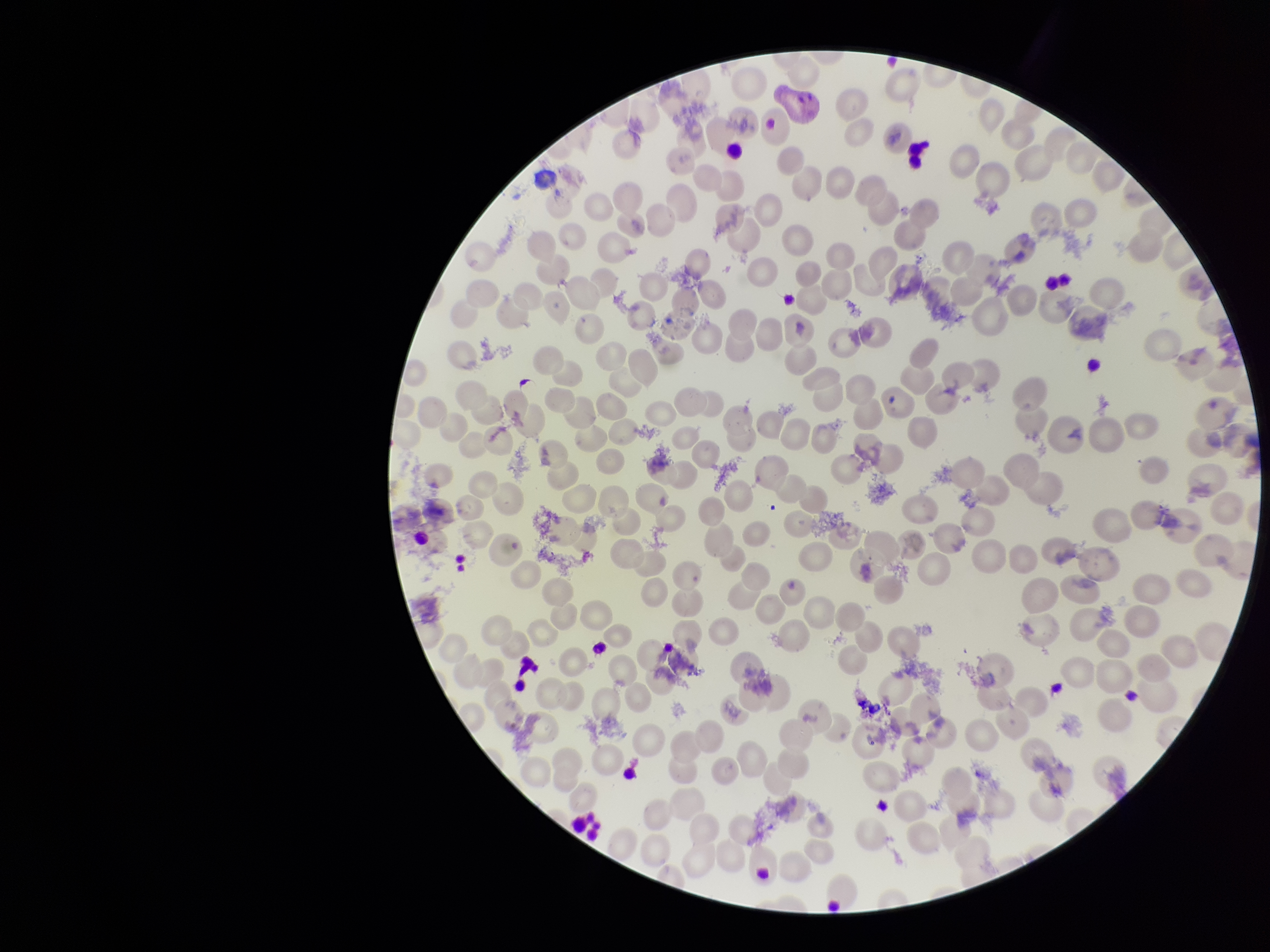

Summary:
  - Field of view: one from this slide
  - Parasitized red blood cell count: 0
  - Patient malaria status: infected
  - Preparation: thin blood smear
  - Stain: Giemsa
  - Species reported for this patient: Plasmodium vivax
  - Parasitized red blood cells: none identified
  - Image size: 1270×952 pixels
  - Red blood cell count: 216
  - Capture: smartphone photograph through the microscope eyepiece